Report the malaria status of this cell.
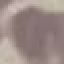

Uninfected.

Acquired by smartphone through the microscope eyepiece. Thin blood smear. Automatically extracted cell patch, resized to 64 × 64 pixels. Giemsa stain.